Assess the morphology of the erythrocytes.
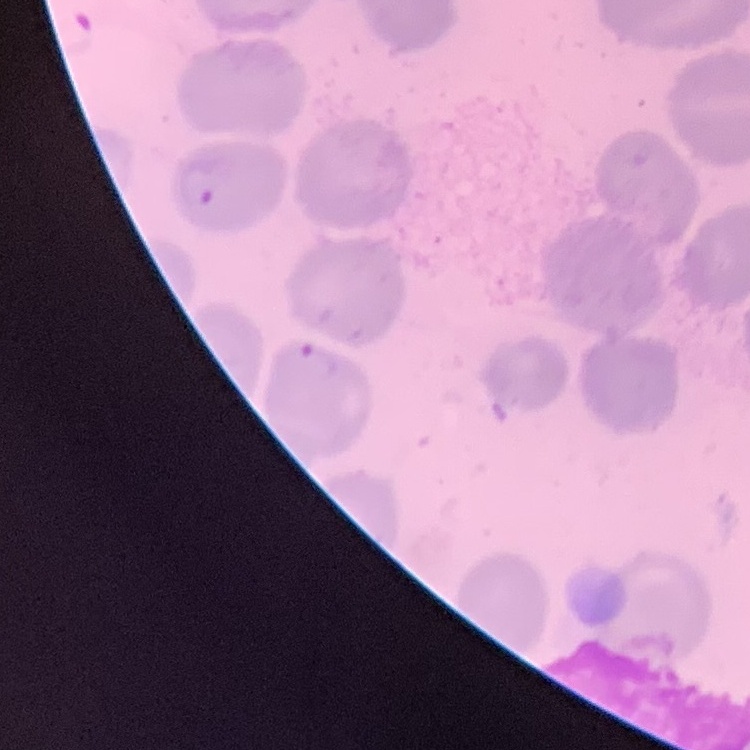
They show no rouleaux formation.

Thin blood film. Stained with either Field's or Giemsa. One tile cut from a larger photomicrograph.